Outline each blood parasite and name the species.
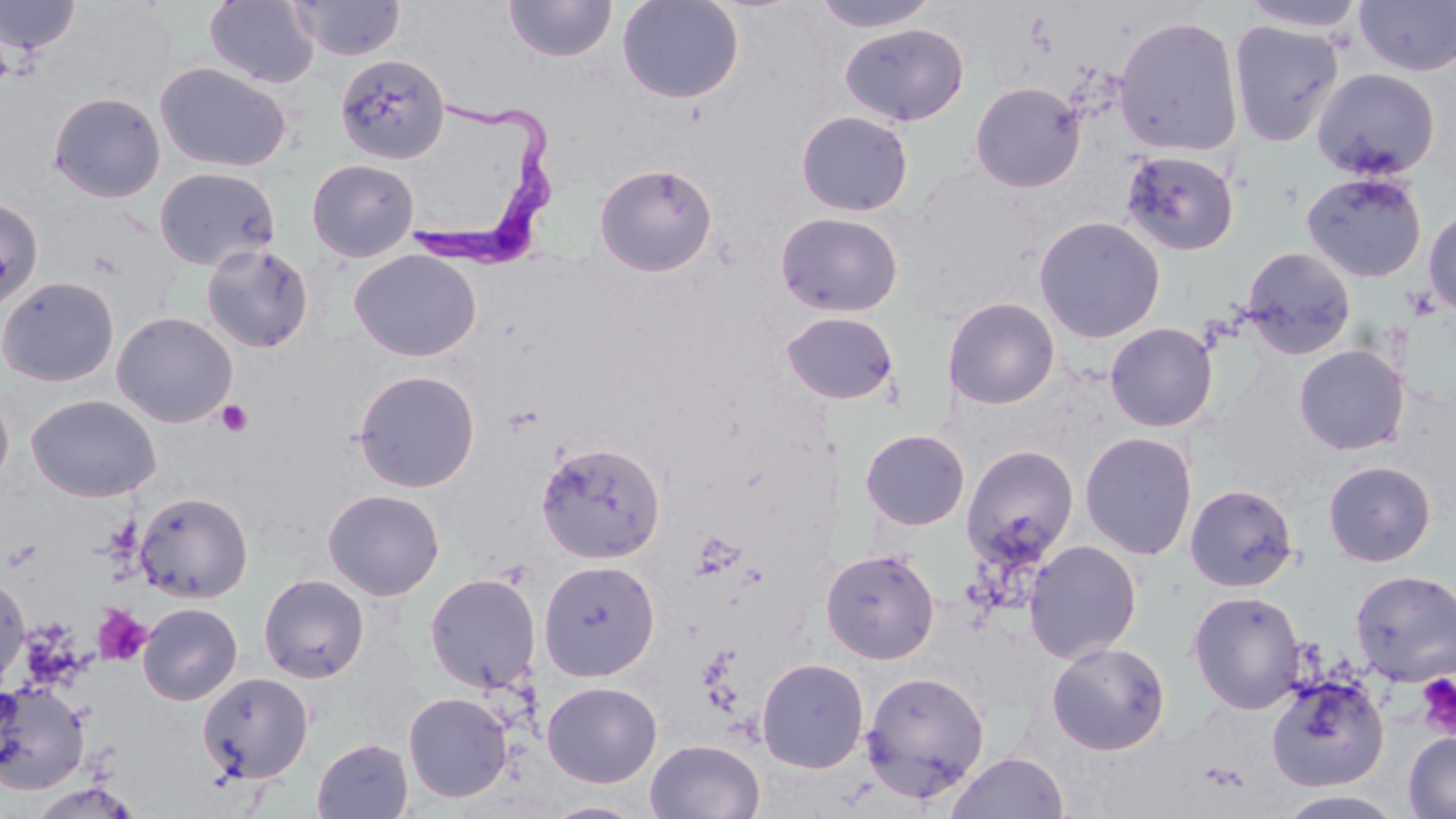

Approximate bounding boxes as (x1, y1, x2, y2) in pixels.
Trypanosoma brucei: (403, 89, 558, 275).
No Plasmodium falciparum, Plasmodium ovale, Plasmodium malariae, Plasmodium vivax, or Babesia divergens observed.

Platelet locations: (216, 400, 254, 437), (92, 605, 153, 667), (1416, 672, 1456, 739). Uninfected red blood cell locations: (0, 0, 82, 57), (205, 0, 319, 88), (292, 0, 404, 60), (504, 0, 617, 63), (616, 0, 745, 105), (809, 0, 940, 33), (1238, 0, 1368, 34), (1354, 0, 1456, 77), (1113, 14, 1244, 158), (1227, 19, 1345, 148), (840, 22, 969, 126), (334, 52, 450, 165), (154, 62, 292, 173), (1312, 67, 1441, 182), (969, 80, 1086, 193), (48, 91, 166, 203), (795, 110, 914, 216), (1119, 150, 1240, 256), (307, 158, 419, 262), (593, 162, 718, 277), (154, 166, 280, 272), (1300, 170, 1428, 282), (0, 197, 44, 310), (1423, 207, 1456, 317), (775, 211, 903, 317), (1033, 215, 1166, 343), (200, 242, 314, 353), (1240, 246, 1356, 359), (348, 249, 483, 362), (0, 276, 120, 388), (942, 296, 1061, 409), (111, 311, 238, 427), (780, 311, 899, 405), (1104, 322, 1219, 432), (1293, 344, 1410, 455), (353, 369, 481, 493), (0, 387, 15, 494), (25, 394, 162, 503), (859, 428, 971, 531), (1079, 431, 1198, 561), (536, 441, 666, 565), (961, 444, 1080, 564), (1323, 460, 1436, 567), (1185, 483, 1299, 592), (322, 488, 445, 601), (134, 491, 253, 603), (1023, 539, 1143, 664), (820, 547, 940, 665), (538, 559, 661, 682), (1349, 569, 1456, 686), (0, 570, 30, 690), (258, 573, 369, 683), (424, 573, 541, 693), (1188, 589, 1307, 714), (137, 602, 243, 705), (1046, 641, 1171, 755), (756, 657, 869, 773), (860, 669, 990, 801), (197, 672, 315, 784), (1265, 672, 1389, 791), (0, 680, 89, 794), (541, 680, 663, 788), (403, 691, 513, 803), (1403, 731, 1456, 818), (312, 738, 414, 818), (645, 738, 766, 819), (944, 750, 1069, 819), (1277, 790, 1408, 818), (540, 799, 653, 818). Slide-level diagnosis: Trypanosoma brucei. Single field of view. Captured at 1000x magnification. Thin blood film. May-Grünwald-Giemsa stain. Image is 1456×819 pixels. Light microscopy.